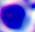

A leukocyte is seen. Captured at 400x magnification. Photomicrograph.